Classify this cell by malaria status.
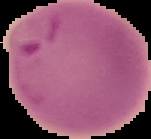

It is parasitized.

Image is 151×139 pixels. Segmented cell region on a black background. From a thin blood film.